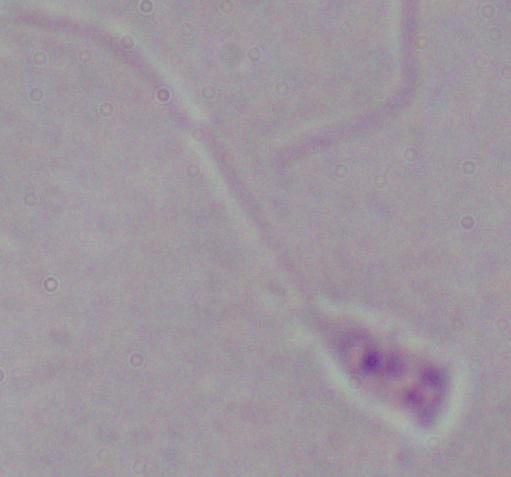
Summary:
  - Modality: micrograph
  - Identification: Leishmania
  - Magnification: 1000x